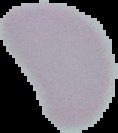 Malaria status: uninfected. From a thin blood smear. Image is 118×133 pixels. Cell region segmented out of the field of view; the surrounding area is masked to black.